Assess the morphology of the red blood cells.
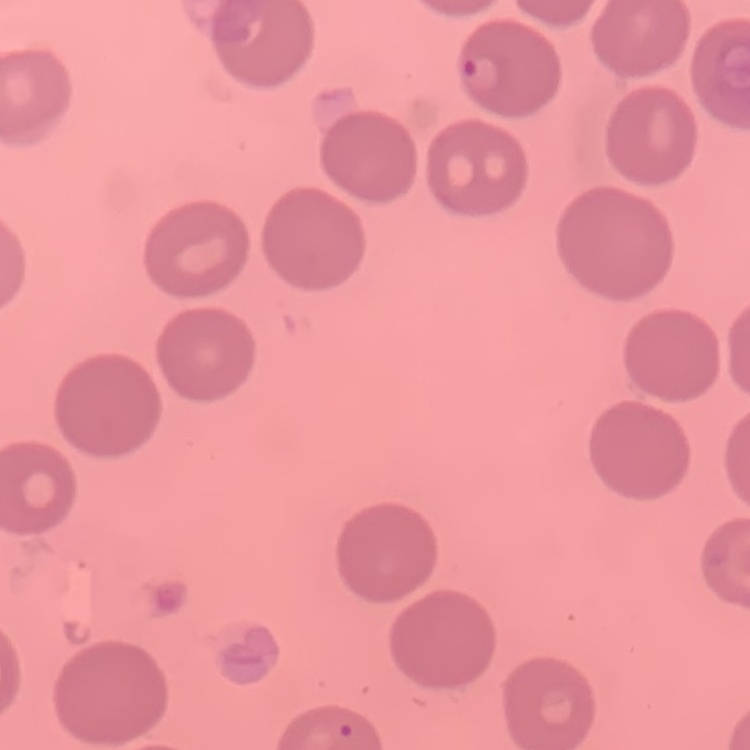
No rouleaux formation.

Summary:
  - Stain: Field's or Giemsa
  - Image type: one tile cut from a larger photomicrograph
  - Preparation: thin peripheral smear